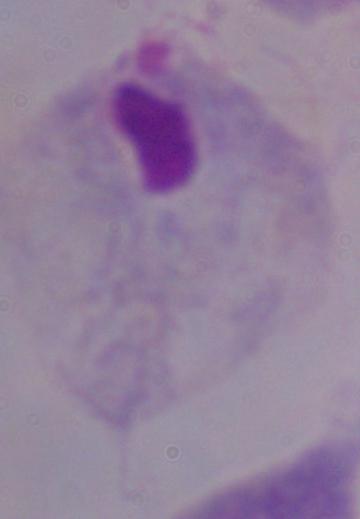

identification = trichomonad
modality = photomicrograph
magnification = 1000x